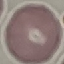
{
  "malaria_status": "uninfected",
  "capture": "smartphone through the microscope eyepiece",
  "preparation": "thin smear",
  "stain": "Giemsa",
  "image_type": "cell patch, automatically extracted from a larger field of view and resized to 64 × 64 pixels"
}